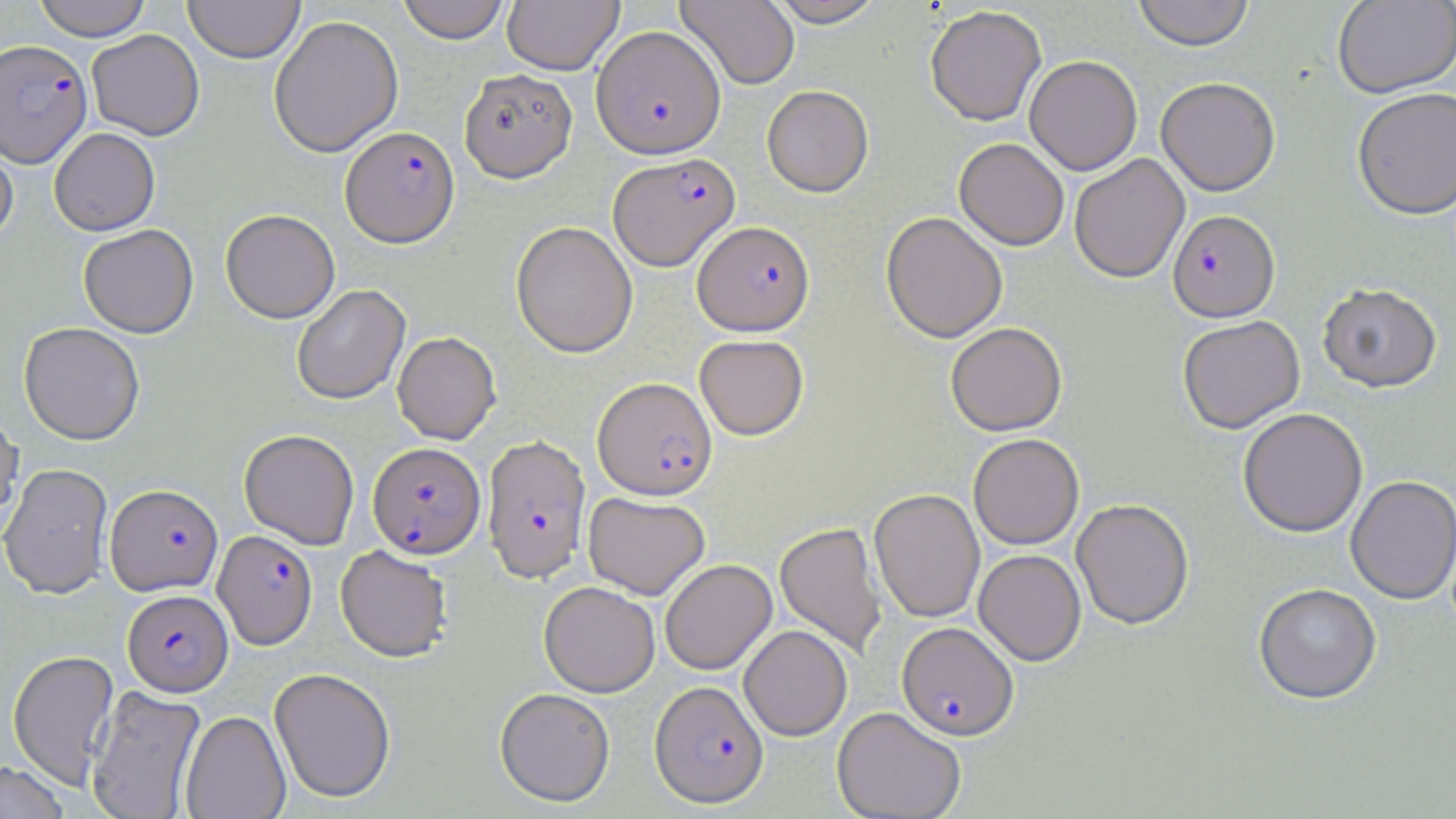

Summary:
  - Coordinate format: approximate bounding boxes as named x1/y1/x2/y2 corners in pixels
  - Plasmodium falciparum-infected red blood cell locations (subset): (x1=1, y1=39, x2=92, y2=168), (x1=340, y1=125, x2=459, y2=248), (x1=608, y1=152, x2=739, y2=270), (x1=1167, y1=209, x2=1279, y2=322), (x1=693, y1=220, x2=814, y2=335), (x1=593, y1=376, x2=716, y2=499), (x1=482, y1=434, x2=591, y2=583), (x1=368, y1=441, x2=486, y2=559), (x1=105, y1=485, x2=223, y2=596), (x1=213, y1=530, x2=317, y2=650), (x1=122, y1=589, x2=233, y2=696), (x1=897, y1=622, x2=1019, y2=740), (x1=650, y1=680, x2=769, y2=808)
  - Uninfected red blood cell locations (subset): (x1=33, y1=0, x2=151, y2=41), (x1=183, y1=0, x2=305, y2=63), (x1=397, y1=0, x2=511, y2=44), (x1=675, y1=0, x2=800, y2=90), (x1=766, y1=0, x2=887, y2=26), (x1=1132, y1=0, x2=1255, y2=50), (x1=1332, y1=0, x2=1456, y2=98), (x1=502, y1=1, x2=623, y2=74), (x1=925, y1=6, x2=1047, y2=126), (x1=269, y1=14, x2=403, y2=158), (x1=86, y1=29, x2=204, y2=140), (x1=1024, y1=55, x2=1142, y2=175), (x1=459, y1=68, x2=577, y2=182), (x1=1156, y1=77, x2=1280, y2=195), (x1=762, y1=85, x2=873, y2=197), (x1=1352, y1=86, x2=1456, y2=220), (x1=0, y1=124, x2=19, y2=247), (x1=49, y1=128, x2=160, y2=236), (x1=954, y1=137, x2=1069, y2=250), (x1=1070, y1=154, x2=1189, y2=283), (x1=220, y1=210, x2=340, y2=324), (x1=881, y1=211, x2=1007, y2=343), (x1=511, y1=221, x2=638, y2=358), (x1=79, y1=225, x2=198, y2=339), (x1=1317, y1=282, x2=1442, y2=392), (x1=292, y1=285, x2=411, y2=405), (x1=1177, y1=315, x2=1304, y2=433), (x1=18, y1=322, x2=145, y2=446), (x1=946, y1=322, x2=1067, y2=436), (x1=392, y1=331, x2=501, y2=445), (x1=694, y1=334, x2=809, y2=439), (x1=1237, y1=407, x2=1368, y2=537), (x1=0, y1=410, x2=24, y2=532), (x1=239, y1=429, x2=359, y2=549), (x1=969, y1=433, x2=1084, y2=549), (x1=1, y1=463, x2=114, y2=600), (x1=1345, y1=475, x2=1456, y2=604), (x1=869, y1=488, x2=985, y2=622), (x1=583, y1=491, x2=710, y2=600), (x1=1071, y1=498, x2=1194, y2=628), (x1=775, y1=522, x2=886, y2=657), (x1=335, y1=545, x2=453, y2=663), (x1=973, y1=549, x2=1086, y2=666), (x1=660, y1=559, x2=777, y2=675), (x1=539, y1=581, x2=660, y2=697), (x1=1254, y1=583, x2=1381, y2=704), (x1=739, y1=625, x2=852, y2=741), (x1=7, y1=649, x2=120, y2=791), (x1=269, y1=667, x2=396, y2=804), (x1=86, y1=686, x2=206, y2=819), (x1=495, y1=687, x2=615, y2=806), (x1=832, y1=706, x2=966, y2=819), (x1=180, y1=710, x2=291, y2=819), (x1=0, y1=761, x2=70, y2=819)
  - Slide-level diagnosis: Plasmodium falciparum
  - Stain: May-Grünwald-Giemsa
  - Image size: 1456×819 pixels
  - Modality: light microscopy
  - Preparation: thin blood smear
  - Magnification: 1000x
  - Field of view: single